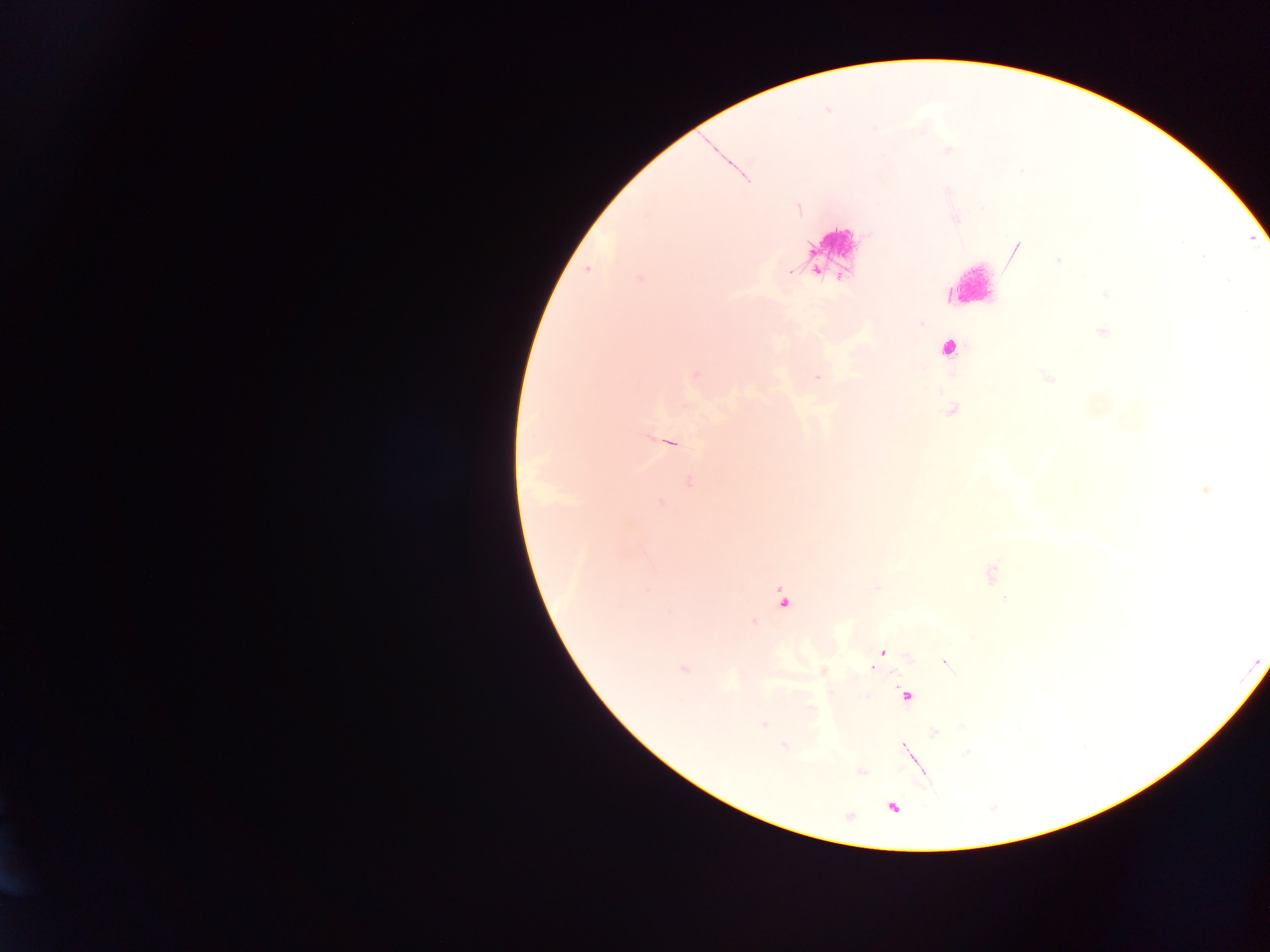
field of view = single
malaria parasite locations = approximate centers as {x, y} in pixels: {586, 269}, {787, 272}, {817, 376}, {876, 588}, {646, 590}, {783, 603}, {753, 621}, {872, 670}, {909, 695}, {785, 746}, {862, 772}, {850, 818}
capture = mobile-phone photograph through a microscope
image size = 1270×952 pixels
preparation = thick blood film
country = Ghana